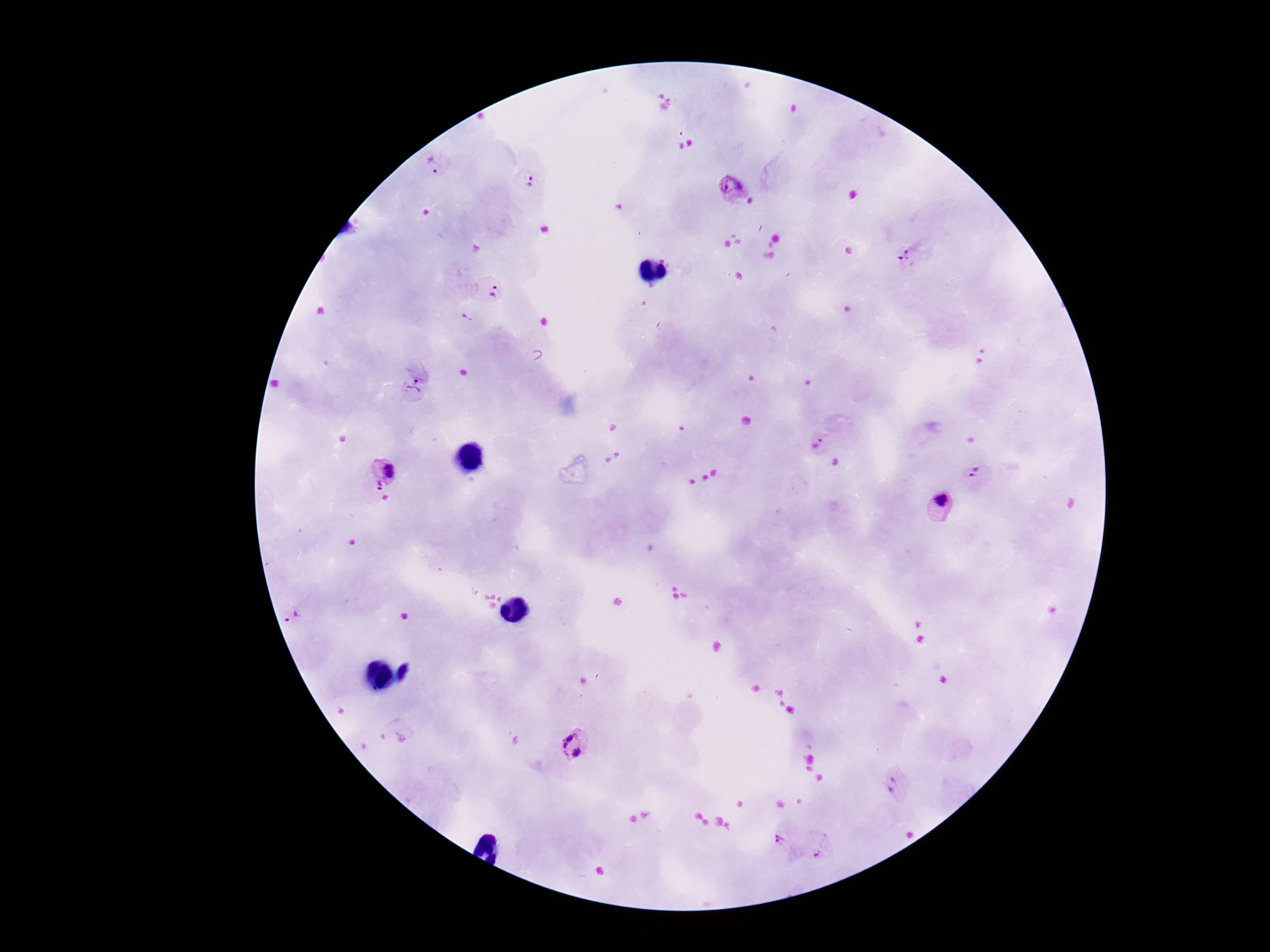

{
  "plasmodium_parasite_locations": "approximate centers as [x, y] in pixels: [433, 166], [529, 186], [735, 189], [907, 259], [483, 293], [416, 389], [817, 444], [382, 472], [981, 479], [937, 508], [297, 618], [575, 746], [898, 790], [782, 836], [820, 845]",
  "magnification": "100x",
  "patient_malaria_status": "infected",
  "field_of_view": "one from this slide",
  "preparation": "thick blood film",
  "capture": "smartphone camera through the microscope eyepiece",
  "image_size": "1270×952 pixels",
  "stain": "Giemsa"
}